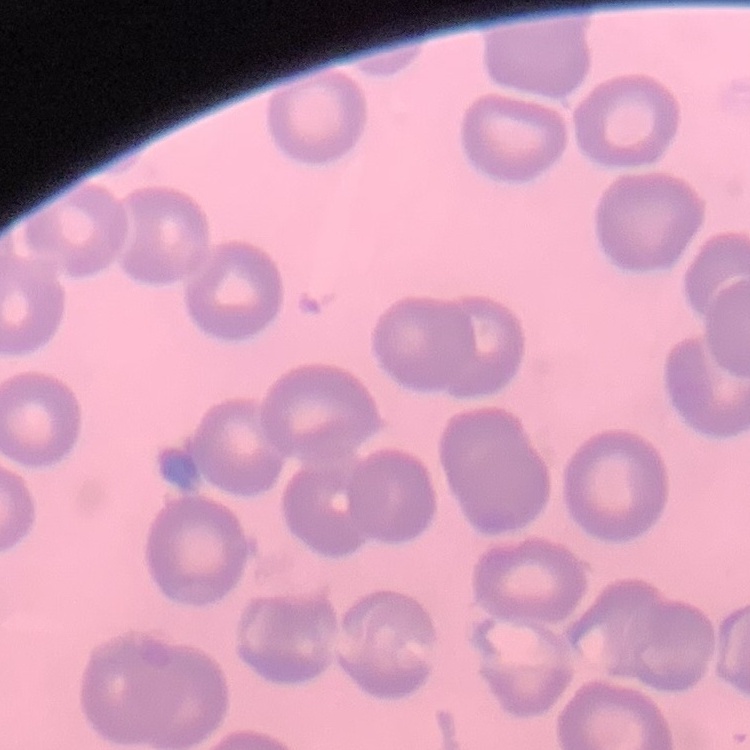 The erythrocytes exhibit no rouleaux formation. Thin blood smear. Square crop of a larger photomicrograph. Field's or Giemsa stain.